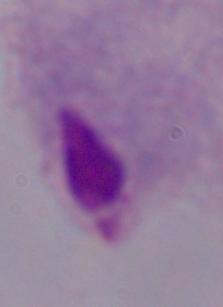

magnification = 1000x
identification = trichomonad
modality = micrograph